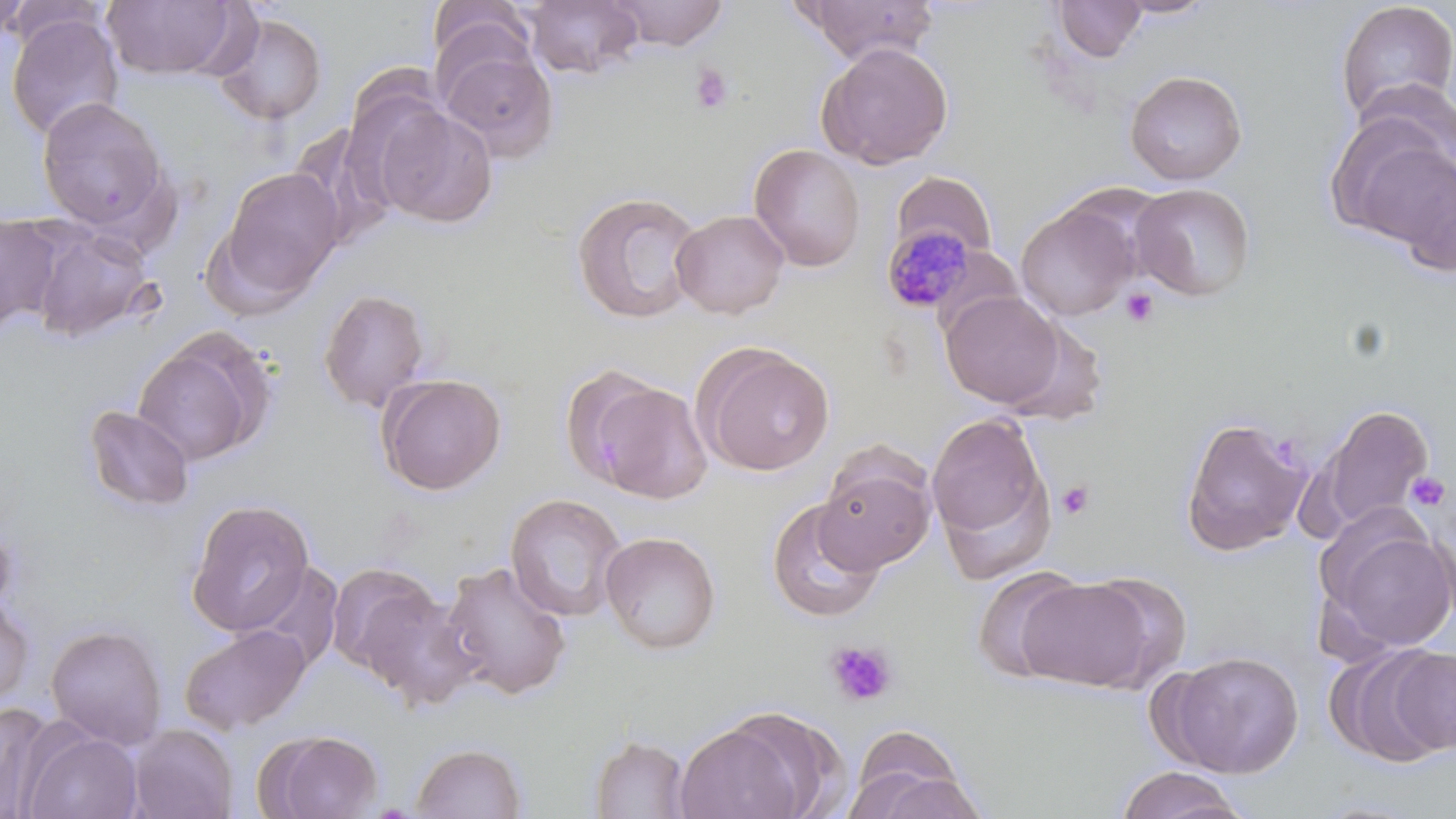
Summary:
  - Coordinate format: approximate bounding boxes as [x1, y1, x2, y2] in pixels
  - Platelet locations: [690, 64, 733, 114], [1120, 287, 1159, 329], [1406, 471, 1451, 513], [1056, 479, 1094, 520], [826, 639, 898, 707]
  - Plasmodium malariae-infected red blood cell locations: [881, 225, 981, 314]
  - Uninfected red blood cell locations: [0, 0, 105, 51], [0, 0, 31, 45], [521, 0, 645, 79], [1111, 0, 1218, 19], [102, 1, 244, 80], [429, 1, 537, 81], [607, 1, 730, 51], [800, 1, 940, 64], [1052, 1, 1148, 62], [1334, 1, 1455, 125], [211, 11, 328, 126], [5, 14, 125, 141], [435, 35, 560, 162], [816, 41, 954, 170], [1124, 69, 1248, 186], [36, 97, 170, 233], [370, 104, 499, 229], [1329, 118, 1454, 248], [748, 143, 866, 272], [1384, 151, 1456, 274], [212, 166, 344, 305], [892, 171, 997, 264], [1130, 183, 1256, 302], [571, 190, 704, 325], [1015, 203, 1137, 321], [671, 208, 790, 319], [0, 212, 65, 333], [28, 223, 158, 343], [318, 287, 433, 413], [940, 290, 1066, 409], [133, 335, 266, 467], [696, 343, 835, 477], [377, 372, 507, 496], [584, 380, 713, 504], [1314, 403, 1434, 533], [82, 405, 196, 513], [926, 412, 1054, 564], [1178, 414, 1314, 557], [816, 455, 936, 573], [505, 493, 627, 622], [766, 497, 886, 625], [186, 498, 316, 637], [1322, 525, 1456, 653], [600, 531, 722, 654], [440, 560, 573, 700], [240, 563, 346, 673], [326, 563, 445, 679], [973, 566, 1089, 684], [1077, 570, 1193, 687], [1015, 576, 1161, 691], [0, 593, 36, 709], [46, 624, 167, 748], [179, 624, 312, 735], [1328, 645, 1452, 767], [1167, 650, 1304, 778], [0, 701, 58, 819], [673, 720, 809, 819], [847, 722, 974, 819], [127, 723, 238, 819], [21, 728, 143, 819], [257, 728, 384, 818], [589, 735, 694, 818], [411, 742, 528, 818], [1115, 767, 1249, 819]
  - Slide-level diagnosis: Plasmodium malariae
  - Field of view: single
  - Preparation: thin blood film
  - Modality: light microscopy
  - Magnification: 1000x
  - Image size: 1456×819 pixels
  - Stain: May-Grünwald-Giemsa